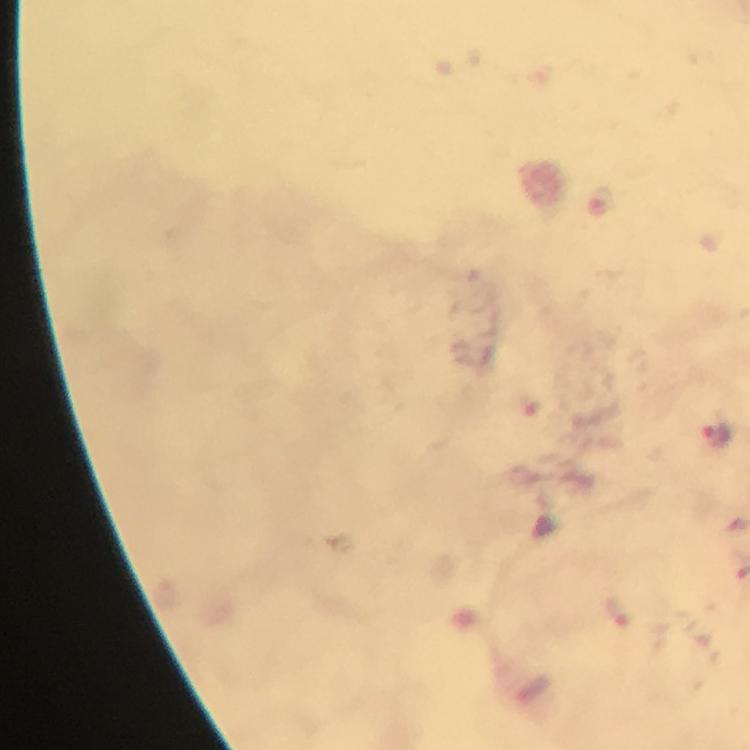

preparation = thick blood smear
context = from a diagnostic examination for malaria
image size = 750×750 pixels
cropped from = one field of view
magnification = 100x
stain = Giemsa
immersion oil = applied
Plasmodium parasite locations = approximate centers as (x, y) in pixels: (714, 432)
capture = smartphone mounted on the microscope